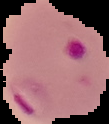
Summary:
  - Image size: 109×124 pixels
  - Preparation: thin blood film
  - Result: Plasmodium parasites identified
  - Image type: cell region segmented out of the field of view; surrounding area masked to black